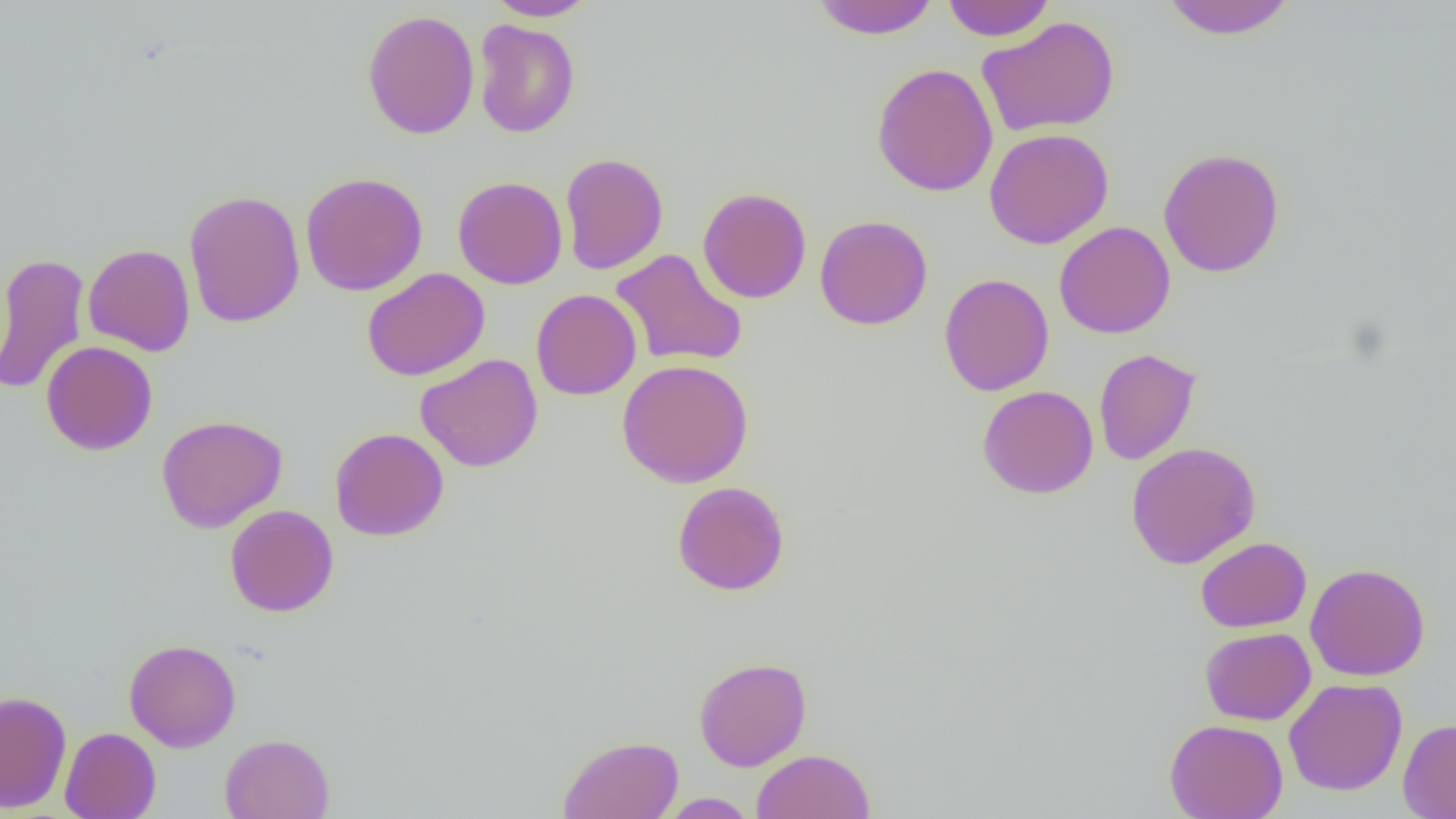

slide_level_diagnosis: negative for blood parasites
uninfected_red_blood_cell_locations: 'approximate bounding boxes as [x1, y1, x2, y2] in pixels: [486, 0, 599, 21], [810, 0, 940, 39], [941, 0, 1054, 42], [1160, 0, 1297, 40], [361, 9, 480, 139], [976, 16, 1121, 137], [473, 19, 580, 138], [871, 62, 998, 197], [984, 128, 1114, 249], [1158, 147, 1286, 278], [559, 152, 668, 275], [300, 171, 428, 296], [452, 175, 568, 289], [697, 187, 812, 303], [183, 189, 306, 328], [814, 214, 933, 330], [1054, 221, 1175, 339], [83, 244, 195, 356], [610, 248, 748, 369], [0, 253, 90, 395], [362, 268, 490, 381], [938, 274, 1055, 396], [531, 289, 642, 400], [41, 341, 158, 456], [1093, 348, 1201, 466], [415, 354, 544, 472], [617, 359, 754, 488], [977, 385, 1099, 499], [155, 414, 288, 533], [330, 427, 449, 541], [1125, 441, 1261, 569], [672, 481, 790, 596], [225, 504, 339, 617], [1196, 536, 1311, 632], [1304, 562, 1431, 682], [1200, 627, 1316, 725], [124, 638, 241, 752], [694, 657, 812, 772], [1284, 677, 1407, 795], [0, 689, 72, 812], [1164, 718, 1289, 818], [1398, 718, 1456, 818], [59, 727, 161, 819], [220, 733, 335, 819], [558, 735, 683, 818], [751, 748, 875, 819], [658, 792, 758, 818]'
preparation: thin blood smear
image_size: 1456×819 pixels
field_of_view: single
modality: optical microscopy
magnification: 1000x